State the blood parasite species.
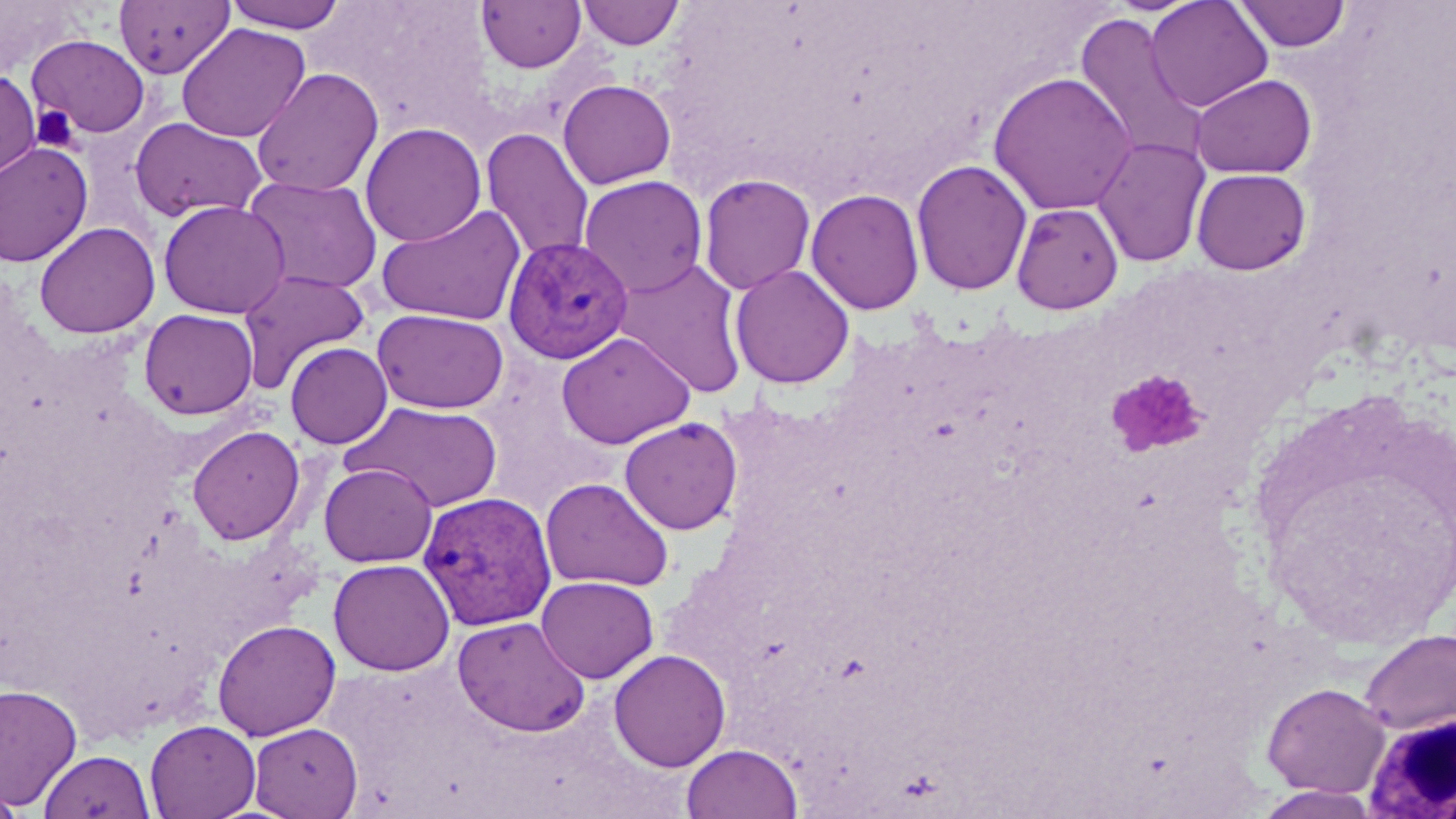
Plasmodium vivax.

magnification = 1000x
modality = optical microscopy
platelet locations = approximate bounding boxes as (x1,y1)-(x2,y2) corner pairs in pixels: (29,103)-(82,153), (1107,369)-(1208,457)
image size = 1456×819 pixels
Plasmodium vivax-infected red blood cell locations = approximate bounding boxes as (x1,y1)-(x2,y2) corner pairs in pixels: (503,237)-(633,364), (418,492)-(557,631)
uninfected red blood cell locations = approximate bounding boxes as (x1,y1)-(x2,y2) corner pairs in pixels: (224,0)-(350,33), (578,0)-(683,49), (1146,0)-(1273,112), (1233,0)-(1352,53), (114,1)-(234,79), (477,1)-(586,73), (1073,12)-(1209,169), (176,23)-(310,143), (27,34)-(150,138), (0,68)-(41,182), (252,68)-(383,197), (988,71)-(1136,216), (1190,73)-(1316,179), (558,79)-(676,189), (129,117)-(267,223), (360,122)-(486,247), (481,127)-(595,263), (1092,137)-(1211,268), (0,141)-(93,267), (911,158)-(1032,296), (1191,168)-(1312,275), (698,173)-(816,295), (242,175)-(384,295), (579,175)-(708,298), (806,188)-(925,315), (158,199)-(291,319), (1011,203)-(1123,314), (376,204)-(527,326), (34,221)-(160,339), (613,257)-(750,399), (729,263)-(855,389), (237,269)-(370,393), (372,307)-(509,414), (138,308)-(258,420), (557,331)-(695,449), (285,342)-(393,449), (345,401)-(503,513), (619,416)-(742,534), (187,426)-(305,545), (319,463)-(437,568), (540,477)-(674,592), (328,558)-(454,676), (536,576)-(658,683), (452,616)-(591,737), (212,619)-(341,740), (1359,628)-(1456,736), (609,649)-(730,771), (0,682)-(82,810), (1262,682)-(1390,797), (145,719)-(261,819), (249,722)-(363,818), (681,742)-(803,819), (38,749)-(153,819), (0,783)-(25,818)
field of view = single
stain = May-Grünwald-Giemsa
white blood cell locations = approximate bounding boxes as (x1,y1)-(x2,y2) corner pairs in pixels: (1360,707)-(1455,816)
preparation = thin blood film